Classify this cell by malaria status.
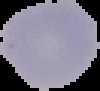

It is uninfected.

Cell region segmented out of the field of view; the surrounding area is masked to black. Image is 100×91 pixels. From a thin blood film.